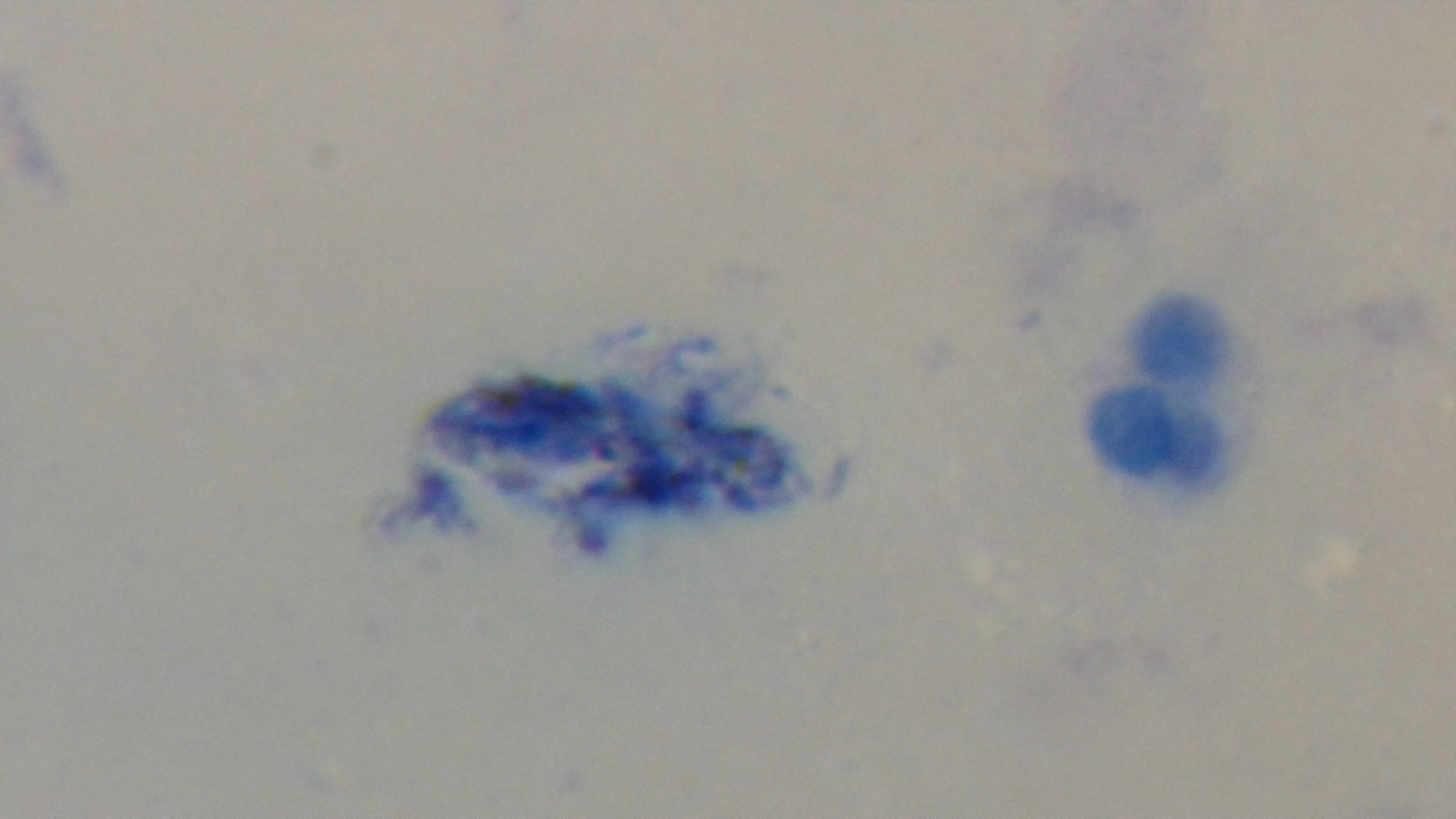
Summary:
  - Capture: mounted 4K digital camera
  - Field of view: single
  - Objective: 100x oil immersion
  - Stain: Giemsa
  - Malaria status: uninfected
  - Modality: light microscopy
  - Preparation: thick